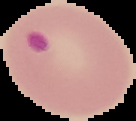
Summary:
  - Preparation: thin blood smear
  - Malaria status: parasitized
  - Image size: 136×121 pixels
  - Image type: segmented cell region on a black background